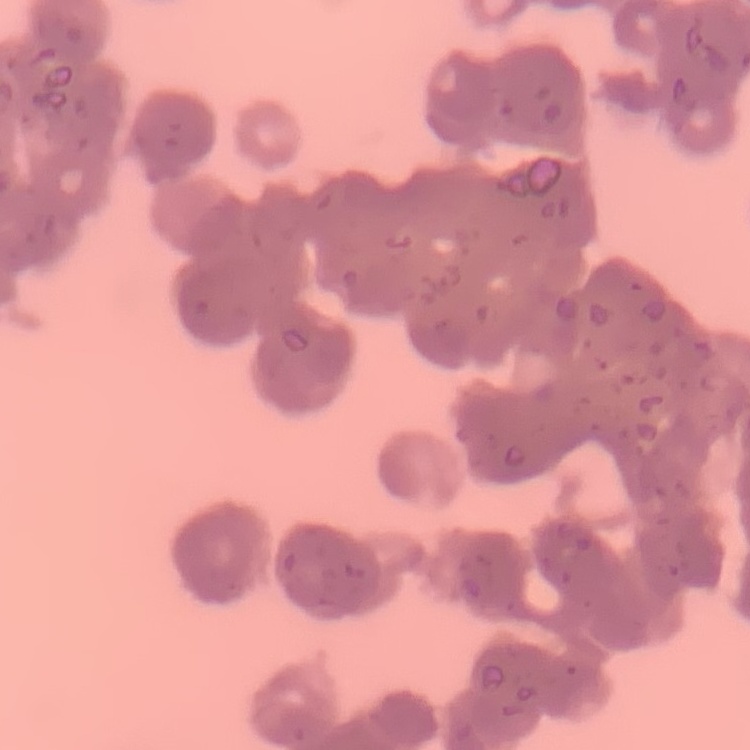 The red blood cells show rouleaux formation. Thin blood smear. Square crop of a larger photomicrograph. Field's or Giemsa stain.